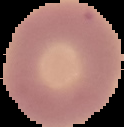
{
  "image_size": "124×127 pixels",
  "preparation": "thin blood film",
  "result": "no malaria parasites detected",
  "image_type": "cell region segmented out of the field of view; surrounding area masked to black"
}